Give the extent of all Plasmodium falciparum-infected red blood cells.
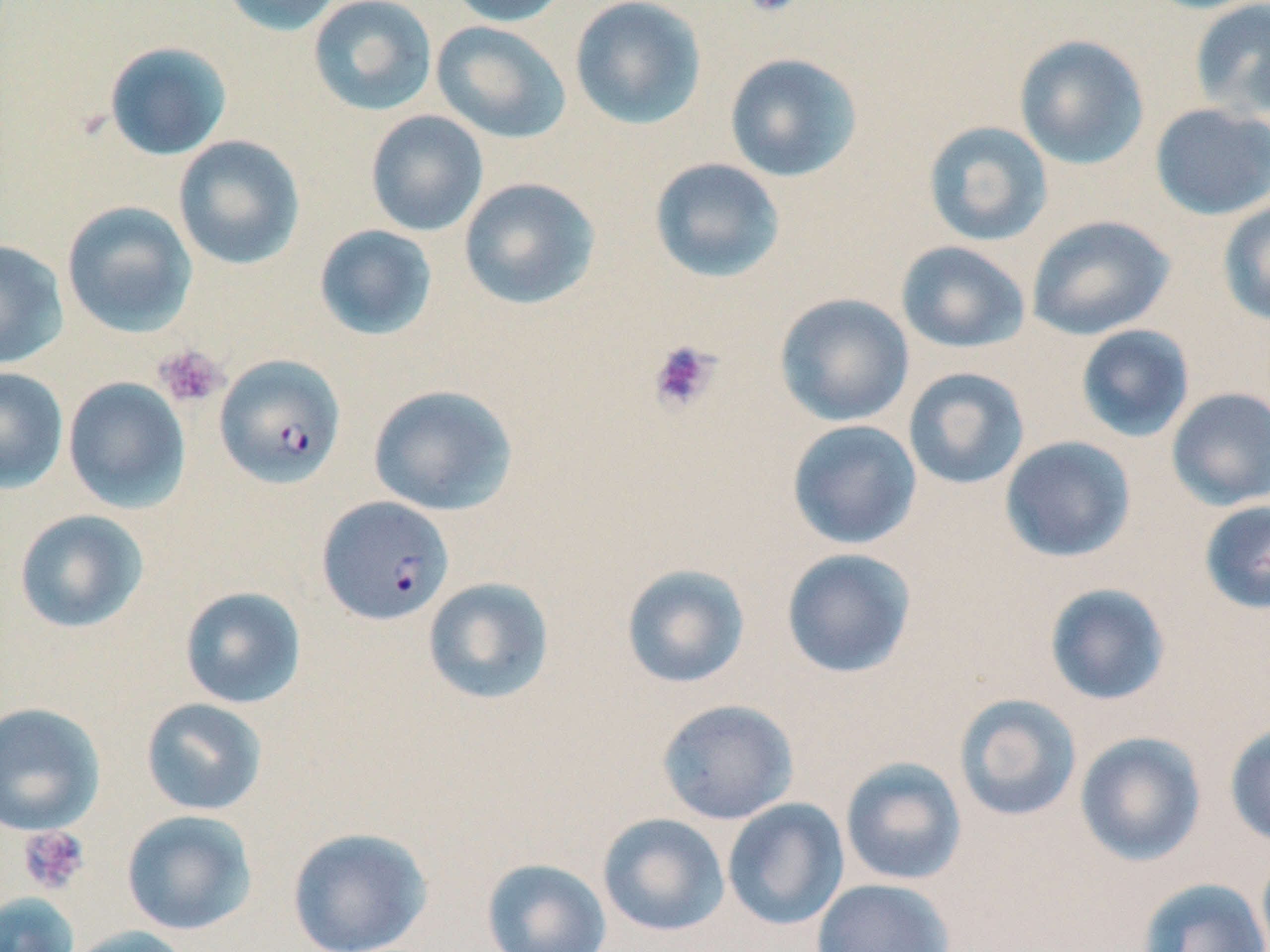
Approximate bounding boxes as named x1/y1/x2/y2 corners in pixels.
Plasmodium falciparum-infected red blood cells: (x1=214, y1=354, x2=346, y2=488), (x1=317, y1=496, x2=454, y2=626).

Uninfected red blood cell locations: (x1=220, y1=0, x2=345, y2=36), (x1=307, y1=0, x2=437, y2=117), (x1=446, y1=0, x2=572, y2=27), (x1=569, y1=0, x2=707, y2=130), (x1=1188, y1=1, x2=1270, y2=122), (x1=430, y1=20, x2=572, y2=144), (x1=1013, y1=34, x2=1150, y2=170), (x1=103, y1=41, x2=232, y2=161), (x1=724, y1=52, x2=864, y2=183), (x1=1149, y1=103, x2=1270, y2=220), (x1=365, y1=110, x2=488, y2=236), (x1=922, y1=121, x2=1053, y2=247), (x1=173, y1=135, x2=306, y2=270), (x1=649, y1=158, x2=786, y2=283), (x1=458, y1=177, x2=601, y2=310), (x1=1217, y1=199, x2=1270, y2=327), (x1=61, y1=201, x2=198, y2=337), (x1=1026, y1=214, x2=1175, y2=341), (x1=313, y1=225, x2=438, y2=341), (x1=0, y1=240, x2=69, y2=369), (x1=895, y1=241, x2=1031, y2=354), (x1=774, y1=293, x2=915, y2=427), (x1=1075, y1=324, x2=1195, y2=443), (x1=0, y1=367, x2=68, y2=493), (x1=902, y1=367, x2=1030, y2=490), (x1=62, y1=377, x2=191, y2=513), (x1=367, y1=384, x2=518, y2=516), (x1=1166, y1=387, x2=1270, y2=510), (x1=786, y1=419, x2=922, y2=550), (x1=1000, y1=435, x2=1136, y2=562), (x1=1199, y1=499, x2=1270, y2=616), (x1=13, y1=509, x2=149, y2=634), (x1=780, y1=548, x2=917, y2=678), (x1=620, y1=563, x2=751, y2=689), (x1=422, y1=576, x2=555, y2=705), (x1=1043, y1=582, x2=1171, y2=706), (x1=179, y1=586, x2=307, y2=709), (x1=954, y1=693, x2=1082, y2=822), (x1=140, y1=697, x2=268, y2=816), (x1=656, y1=699, x2=799, y2=825), (x1=0, y1=702, x2=106, y2=836), (x1=1225, y1=721, x2=1270, y2=849), (x1=1074, y1=731, x2=1207, y2=866), (x1=839, y1=756, x2=968, y2=886), (x1=722, y1=798, x2=850, y2=931), (x1=121, y1=809, x2=258, y2=936), (x1=597, y1=812, x2=730, y2=937), (x1=286, y1=825, x2=433, y2=952), (x1=1256, y1=846, x2=1270, y2=952), (x1=481, y1=858, x2=613, y2=952), (x1=1136, y1=877, x2=1270, y2=952), (x1=811, y1=878, x2=956, y2=952), (x1=0, y1=892, x2=80, y2=952), (x1=65, y1=925, x2=194, y2=952). Platelet locations: (x1=740, y1=0, x2=803, y2=19), (x1=647, y1=339, x2=721, y2=414), (x1=153, y1=345, x2=226, y2=408), (x1=17, y1=825, x2=90, y2=895). Slide-level diagnosis: Plasmodium falciparum. May-Grünwald-Giemsa stain. Image is 1270×952 pixels. One field of a larger specimen. Thin blood film. 1000x magnification. Light microscopy.